Assess this cell for malaria.
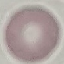
Uninfected.

stain: Giemsa
capture: smartphone through the microscope eyepiece
image_type: cell patch, automatically extracted from a larger field of view and resized to 64 × 64 pixels
preparation: thin smear